Outline each blood parasite and name the species.
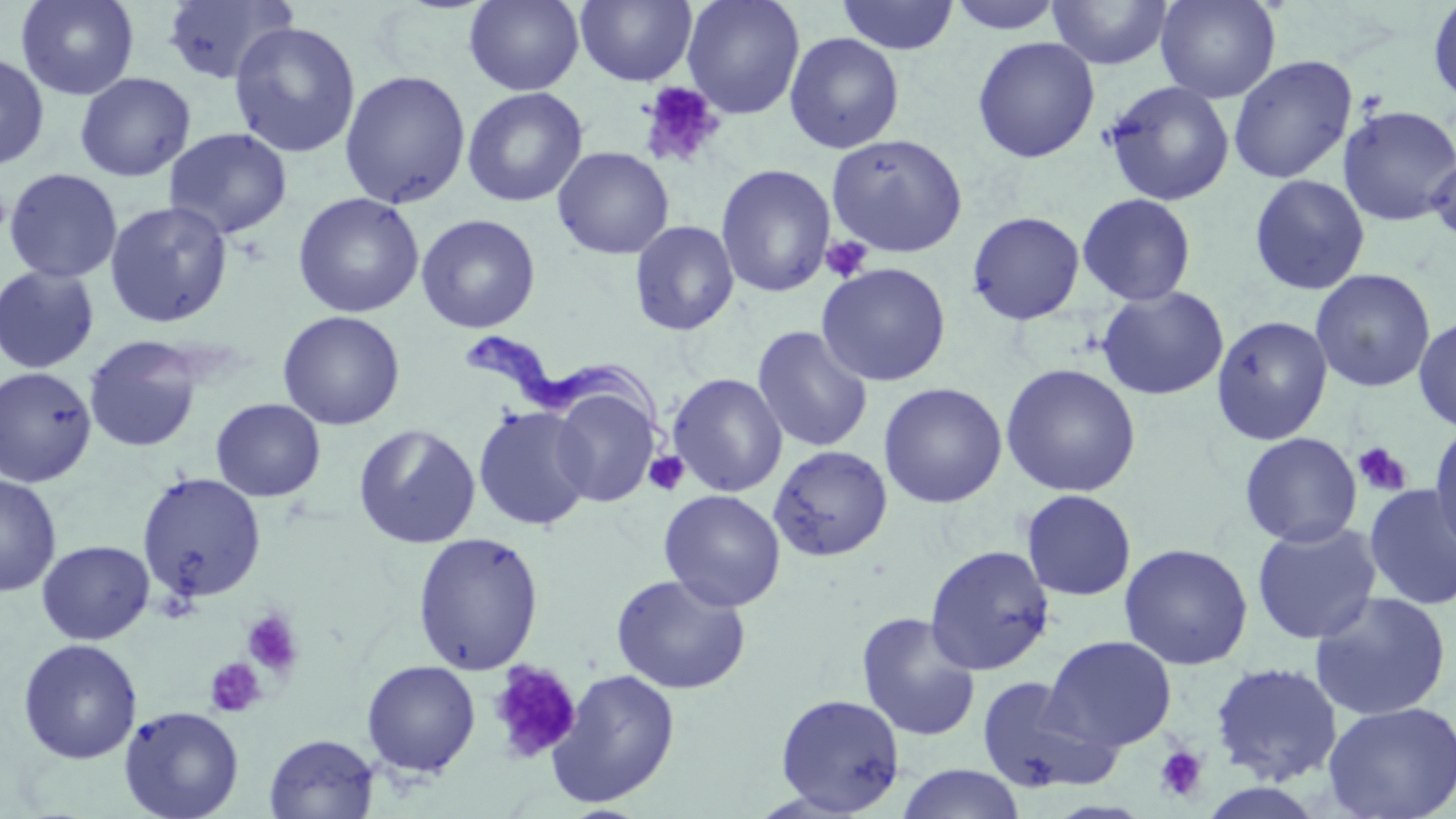
Approximate bounding boxes as named x1/y1/x2/y2 corners in pixels.
Trypanosoma brucei: (x1=462, y1=332, x2=673, y2=441).
No Plasmodium falciparum, Plasmodium ovale, Plasmodium malariae, Plasmodium vivax, or Babesia divergens observed.

slide-level diagnosis = Trypanosoma brucei
uninfected red blood cell locations = approximate bounding boxes as named x1/y1/x2/y2 corners in pixels: (x1=15, y1=0, x2=140, y2=101), (x1=161, y1=0, x2=298, y2=85), (x1=464, y1=0, x2=584, y2=95), (x1=575, y1=0, x2=697, y2=86), (x1=682, y1=0, x2=805, y2=119), (x1=836, y1=0, x2=960, y2=55), (x1=946, y1=0, x2=1065, y2=34), (x1=1046, y1=0, x2=1174, y2=71), (x1=1156, y1=0, x2=1280, y2=103), (x1=1427, y1=0, x2=1456, y2=108), (x1=228, y1=21, x2=361, y2=159), (x1=784, y1=33, x2=905, y2=154), (x1=971, y1=36, x2=1100, y2=163), (x1=0, y1=51, x2=50, y2=171), (x1=1228, y1=54, x2=1357, y2=184), (x1=339, y1=69, x2=471, y2=209), (x1=74, y1=72, x2=196, y2=182), (x1=1103, y1=80, x2=1235, y2=206), (x1=462, y1=87, x2=588, y2=207), (x1=1337, y1=105, x2=1456, y2=226), (x1=164, y1=127, x2=293, y2=239), (x1=826, y1=133, x2=967, y2=257), (x1=552, y1=146, x2=674, y2=259), (x1=1426, y1=148, x2=1456, y2=246), (x1=715, y1=164, x2=836, y2=297), (x1=3, y1=168, x2=123, y2=284), (x1=1248, y1=174, x2=1370, y2=295), (x1=292, y1=192, x2=424, y2=318), (x1=1077, y1=193, x2=1197, y2=306), (x1=104, y1=200, x2=233, y2=328), (x1=967, y1=211, x2=1085, y2=325), (x1=416, y1=214, x2=541, y2=333), (x1=629, y1=221, x2=739, y2=336), (x1=816, y1=262, x2=951, y2=387), (x1=0, y1=265, x2=100, y2=374), (x1=1310, y1=269, x2=1435, y2=393), (x1=1095, y1=286, x2=1230, y2=401), (x1=276, y1=310, x2=405, y2=431), (x1=1211, y1=315, x2=1333, y2=445), (x1=1413, y1=315, x2=1456, y2=433), (x1=752, y1=326, x2=874, y2=453), (x1=84, y1=335, x2=203, y2=452), (x1=1000, y1=363, x2=1141, y2=497), (x1=0, y1=367, x2=97, y2=487), (x1=667, y1=373, x2=787, y2=497), (x1=879, y1=382, x2=1007, y2=509), (x1=550, y1=387, x2=660, y2=507), (x1=210, y1=398, x2=325, y2=502), (x1=473, y1=405, x2=594, y2=531), (x1=1429, y1=421, x2=1456, y2=558), (x1=353, y1=423, x2=480, y2=549), (x1=1239, y1=432, x2=1362, y2=548), (x1=768, y1=445, x2=893, y2=561), (x1=136, y1=472, x2=266, y2=603), (x1=0, y1=475, x2=61, y2=597), (x1=1363, y1=484, x2=1456, y2=610), (x1=659, y1=489, x2=786, y2=612), (x1=1020, y1=490, x2=1136, y2=601), (x1=1251, y1=522, x2=1382, y2=645), (x1=412, y1=532, x2=545, y2=675), (x1=37, y1=540, x2=154, y2=645), (x1=1118, y1=543, x2=1253, y2=670), (x1=924, y1=544, x2=1055, y2=676), (x1=610, y1=573, x2=751, y2=695), (x1=1308, y1=591, x2=1452, y2=722), (x1=856, y1=612, x2=981, y2=742), (x1=1043, y1=635, x2=1177, y2=751), (x1=18, y1=638, x2=142, y2=764), (x1=362, y1=660, x2=480, y2=777), (x1=1209, y1=661, x2=1344, y2=785), (x1=546, y1=669, x2=681, y2=809), (x1=976, y1=675, x2=1120, y2=795), (x1=775, y1=693, x2=906, y2=815), (x1=1321, y1=701, x2=1456, y2=819), (x1=118, y1=705, x2=244, y2=819), (x1=264, y1=734, x2=379, y2=819), (x1=896, y1=764, x2=1025, y2=819)
magnification = 1000x
platelet locations = approximate bounding boxes as named x1/y1/x2/y2 corners in pixels: (x1=638, y1=81, x2=725, y2=170), (x1=1355, y1=89, x2=1389, y2=120), (x1=821, y1=236, x2=873, y2=283), (x1=1352, y1=442, x2=1413, y2=497), (x1=644, y1=451, x2=689, y2=496), (x1=241, y1=608, x2=304, y2=678), (x1=205, y1=657, x2=267, y2=718), (x1=487, y1=661, x2=581, y2=763), (x1=1154, y1=744, x2=1209, y2=803)
image size = 1456×819 pixels
modality = light microscopy
stain = May-Grünwald-Giemsa
preparation = thin blood smear
field of view = one of a larger specimen